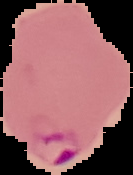

Summary:
  - Image size: 133×175 pixels
  - Preparation: thin blood smear
  - Result: Plasmodium parasites detected
  - Image type: segmented cell region on a black background